Locate every blood parasite and identify its species.
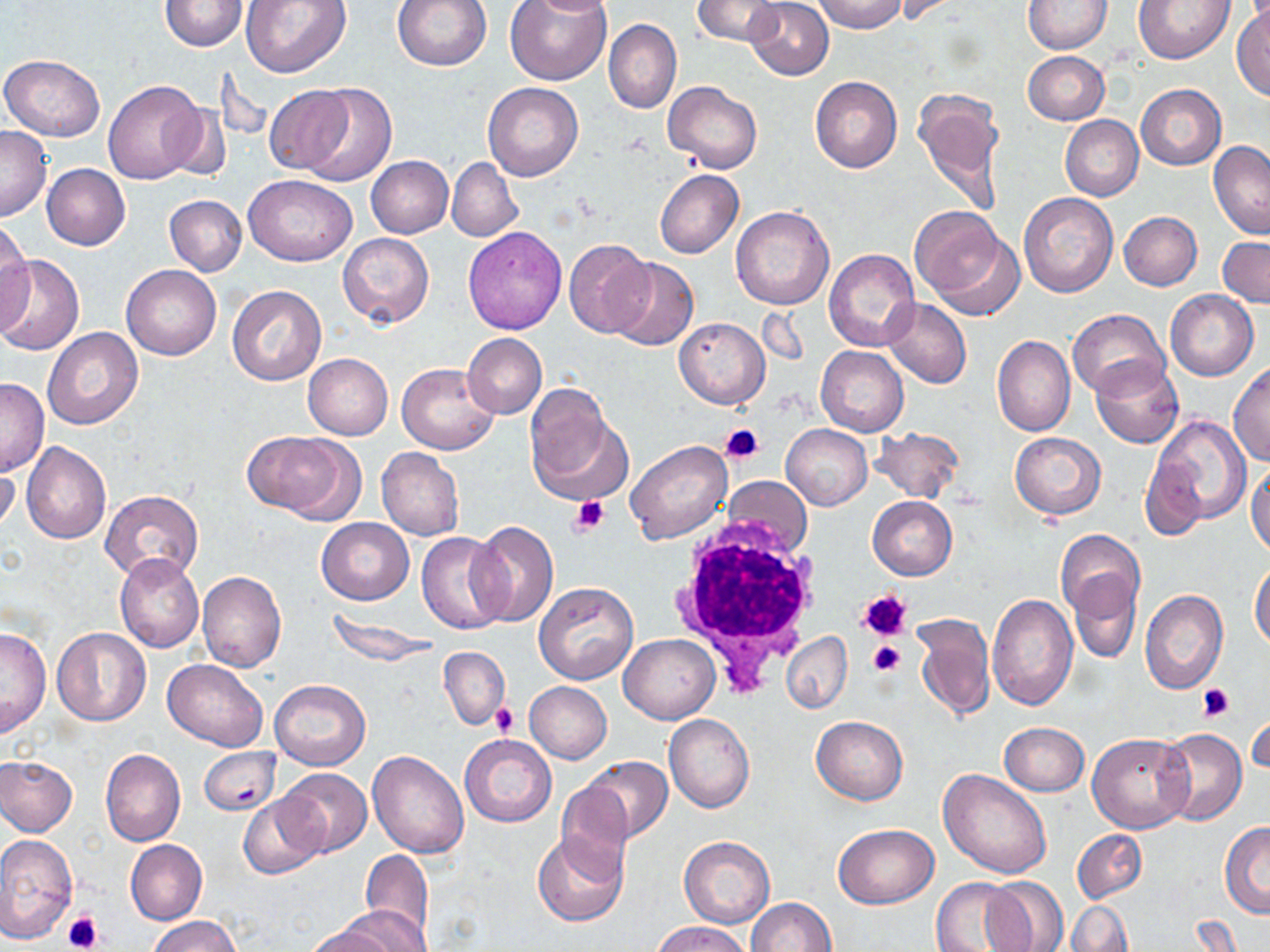
No blood parasites observed.

{
  "slide_level_diagnosis": "no evidence of blood parasites",
  "image_size": "1270×952 pixels",
  "uninfected_red_blood_cell_locations": "approximate bounding boxes as named x1/y1/x2/y2 corners in pixels: (x1=159, y1=0, x2=247, y2=52), (x1=241, y1=0, x2=349, y2=78), (x1=392, y1=0, x2=491, y2=72), (x1=505, y1=0, x2=614, y2=85), (x1=527, y1=0, x2=614, y2=17), (x1=693, y1=0, x2=785, y2=47), (x1=745, y1=0, x2=833, y2=80), (x1=811, y1=0, x2=906, y2=33), (x1=1024, y1=0, x2=1112, y2=53), (x1=1133, y1=0, x2=1235, y2=64), (x1=1233, y1=5, x2=1269, y2=99), (x1=604, y1=19, x2=682, y2=116), (x1=1023, y1=51, x2=1109, y2=125), (x1=0, y1=54, x2=105, y2=140), (x1=810, y1=76, x2=903, y2=173), (x1=103, y1=79, x2=206, y2=184), (x1=663, y1=81, x2=763, y2=173), (x1=298, y1=83, x2=398, y2=187), (x1=484, y1=83, x2=583, y2=181), (x1=1135, y1=84, x2=1226, y2=170), (x1=264, y1=86, x2=356, y2=174), (x1=912, y1=88, x2=1008, y2=214), (x1=162, y1=102, x2=233, y2=182), (x1=1060, y1=115, x2=1143, y2=202), (x1=0, y1=126, x2=51, y2=220), (x1=1208, y1=141, x2=1270, y2=241), (x1=367, y1=155, x2=453, y2=238), (x1=447, y1=157, x2=522, y2=242), (x1=41, y1=163, x2=130, y2=250), (x1=654, y1=170, x2=744, y2=258), (x1=243, y1=175, x2=357, y2=265), (x1=1019, y1=191, x2=1118, y2=297), (x1=164, y1=195, x2=247, y2=276), (x1=731, y1=205, x2=834, y2=311), (x1=909, y1=207, x2=1008, y2=306), (x1=1120, y1=211, x2=1203, y2=291), (x1=0, y1=222, x2=31, y2=327), (x1=462, y1=226, x2=568, y2=334), (x1=337, y1=232, x2=435, y2=329), (x1=1218, y1=236, x2=1270, y2=308), (x1=564, y1=240, x2=655, y2=339), (x1=823, y1=247, x2=919, y2=351), (x1=0, y1=254, x2=84, y2=355), (x1=608, y1=259, x2=696, y2=349), (x1=121, y1=264, x2=221, y2=360), (x1=227, y1=286, x2=328, y2=386), (x1=1166, y1=290, x2=1258, y2=381), (x1=883, y1=298, x2=972, y2=388), (x1=1067, y1=308, x2=1168, y2=398), (x1=674, y1=317, x2=770, y2=409), (x1=44, y1=327, x2=143, y2=429), (x1=462, y1=333, x2=547, y2=419), (x1=993, y1=334, x2=1075, y2=436), (x1=816, y1=346, x2=908, y2=436), (x1=304, y1=354, x2=393, y2=439), (x1=1091, y1=358, x2=1184, y2=448), (x1=396, y1=363, x2=502, y2=454), (x1=1228, y1=363, x2=1270, y2=465), (x1=0, y1=379, x2=49, y2=474), (x1=522, y1=388, x2=628, y2=504), (x1=1152, y1=416, x2=1250, y2=523), (x1=782, y1=425, x2=873, y2=509), (x1=871, y1=426, x2=964, y2=503), (x1=247, y1=430, x2=360, y2=522), (x1=1009, y1=431, x2=1106, y2=518), (x1=625, y1=439, x2=733, y2=544), (x1=21, y1=441, x2=112, y2=544), (x1=376, y1=449, x2=463, y2=541), (x1=0, y1=453, x2=20, y2=537), (x1=1139, y1=454, x2=1207, y2=542), (x1=1248, y1=461, x2=1270, y2=558), (x1=100, y1=490, x2=203, y2=581), (x1=868, y1=495, x2=958, y2=579), (x1=316, y1=517, x2=414, y2=605), (x1=468, y1=520, x2=558, y2=627), (x1=1055, y1=529, x2=1144, y2=620), (x1=416, y1=531, x2=508, y2=635), (x1=114, y1=552, x2=205, y2=654), (x1=1250, y1=562, x2=1270, y2=650), (x1=197, y1=571, x2=287, y2=673), (x1=1070, y1=571, x2=1142, y2=663), (x1=533, y1=582, x2=639, y2=684), (x1=1140, y1=590, x2=1227, y2=694), (x1=986, y1=593, x2=1078, y2=711), (x1=326, y1=611, x2=442, y2=666), (x1=912, y1=614, x2=994, y2=721), (x1=0, y1=626, x2=51, y2=738), (x1=52, y1=627, x2=150, y2=727), (x1=619, y1=633, x2=720, y2=724), (x1=782, y1=633, x2=852, y2=712), (x1=440, y1=646, x2=510, y2=729), (x1=162, y1=658, x2=268, y2=750), (x1=271, y1=679, x2=370, y2=770), (x1=524, y1=682, x2=612, y2=763), (x1=1248, y1=705, x2=1269, y2=778), (x1=664, y1=714, x2=755, y2=812), (x1=811, y1=715, x2=908, y2=804), (x1=998, y1=722, x2=1089, y2=796), (x1=1159, y1=728, x2=1246, y2=825), (x1=1086, y1=732, x2=1194, y2=832), (x1=459, y1=734, x2=556, y2=827), (x1=200, y1=746, x2=279, y2=817), (x1=100, y1=747, x2=186, y2=846), (x1=368, y1=750, x2=469, y2=858), (x1=0, y1=756, x2=77, y2=837), (x1=582, y1=756, x2=673, y2=842), (x1=278, y1=768, x2=372, y2=858), (x1=938, y1=768, x2=1050, y2=878), (x1=556, y1=783, x2=634, y2=879), (x1=239, y1=794, x2=326, y2=881), (x1=1219, y1=821, x2=1270, y2=919), (x1=832, y1=823, x2=938, y2=908), (x1=1072, y1=829, x2=1147, y2=905), (x1=533, y1=831, x2=629, y2=927), (x1=0, y1=833, x2=77, y2=942), (x1=679, y1=836, x2=774, y2=927), (x1=125, y1=839, x2=207, y2=925), (x1=359, y1=848, x2=434, y2=946), (x1=981, y1=875, x2=1069, y2=952), (x1=931, y1=876, x2=1027, y2=952), (x1=745, y1=898, x2=836, y2=952), (x1=1064, y1=900, x2=1133, y2=952), (x1=340, y1=908, x2=427, y2=952), (x1=149, y1=916, x2=241, y2=952), (x1=654, y1=921, x2=749, y2=952), (x1=303, y1=926, x2=394, y2=952)",
  "platelet_locations": "approximate bounding boxes as named x1/y1/x2/y2 corners in pixels: (x1=721, y1=423, x2=763, y2=463), (x1=571, y1=496, x2=609, y2=537), (x1=859, y1=588, x2=913, y2=639), (x1=867, y1=640, x2=905, y2=677), (x1=1197, y1=684, x2=1236, y2=722), (x1=493, y1=703, x2=519, y2=737), (x1=1249, y1=712, x2=1269, y2=772), (x1=63, y1=909, x2=104, y2=951)",
  "preparation": "thin blood smear",
  "field_of_view": "one of a larger specimen",
  "modality": "optical microscopy",
  "white_blood_cell_locations": "approximate bounding boxes as named x1/y1/x2/y2 corners in pixels: (x1=668, y1=513, x2=826, y2=689)",
  "magnification": "1000x",
  "stain": "May-Grünwald-Giemsa"
}